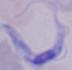
magnification = 1000x
identification = trypanosome
modality = photomicrograph